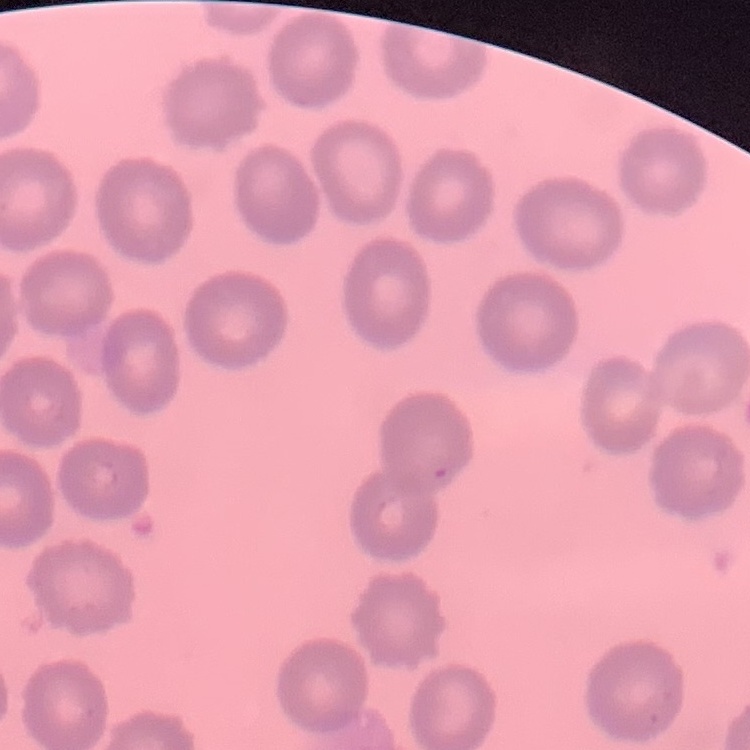

The erythrocytes show no rouleaux formation. Square crop of a larger photomicrograph. Thin blood smear. Field's or Giemsa stain.